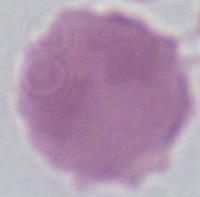

Summary:
  - Identification: erythrocyte
  - Modality: micrograph
  - Magnification: 1000x